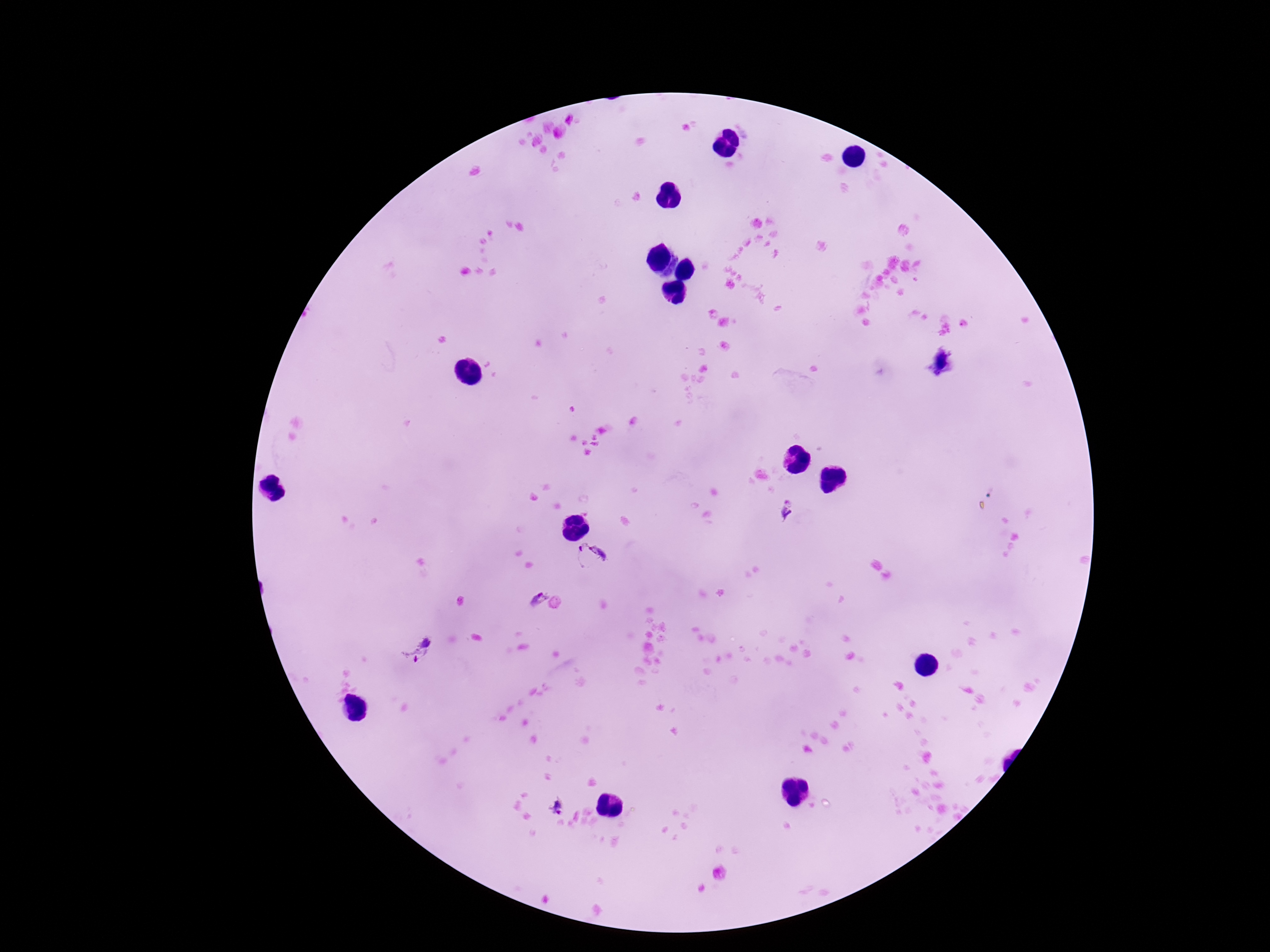

preparation: thick blood film
plasmodium_parasite_locations: 'approximate centers as (x, y) in pixels: (941, 362), (787, 508), (592, 556), (539, 598), (416, 652), (558, 808)'
patient_malaria_status: infected
magnification: 100x
stain: Giemsa
field_of_view: one from this slide
capture: smartphone camera through the microscope eyepiece
image_size: 1270×952 pixels